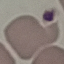
Malaria status: uninfected. Automatically extracted cell patch, resized to 64 × 64 pixels. Photographed with a smartphone camera at the microscope eyepiece. Giemsa stain. Thin blood film.